Classify this cell by malaria status.
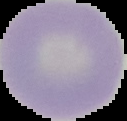
Uninfected.

From a thin blood smear. Segmented cell region on a black background. Image is 127×121 pixels.